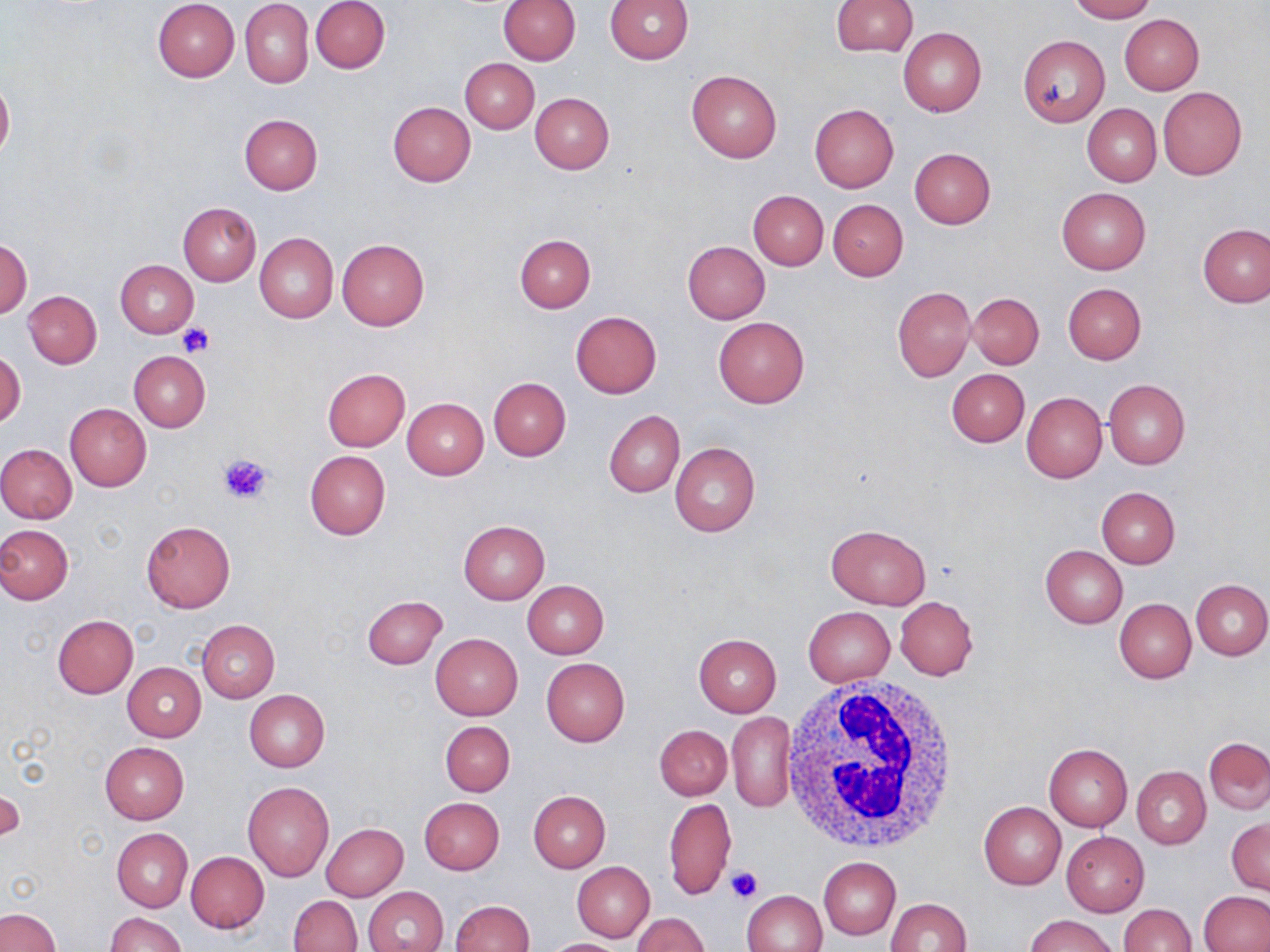

Approximate bounding boxes as (x1, y1, x2, y2) in pixels. Uninfected red blood cell locations: (152, 0, 240, 81), (312, 0, 390, 73), (498, 0, 581, 65), (606, 0, 695, 64), (831, 0, 918, 56), (1070, 0, 1154, 22), (241, 1, 313, 88), (1119, 15, 1204, 95), (898, 26, 986, 117), (1018, 36, 1109, 126), (460, 58, 539, 133), (686, 69, 782, 163), (0, 75, 13, 164), (1158, 87, 1247, 179), (531, 92, 614, 174), (388, 101, 475, 186), (809, 104, 898, 193), (1082, 104, 1161, 187), (239, 114, 323, 194), (909, 148, 996, 229), (1056, 187, 1151, 273), (748, 190, 828, 269), (828, 199, 908, 281), (179, 202, 260, 285), (1199, 224, 1269, 306), (255, 232, 337, 323), (514, 235, 595, 313), (0, 237, 32, 319), (337, 239, 430, 329), (682, 241, 770, 323), (115, 260, 198, 337), (1063, 282, 1147, 364), (892, 287, 975, 382), (24, 291, 101, 368), (969, 293, 1044, 369), (571, 311, 662, 398), (714, 316, 809, 407), (1, 350, 24, 429), (128, 351, 211, 432), (322, 369, 410, 451), (947, 369, 1028, 447), (488, 377, 571, 460), (1104, 378, 1190, 469), (1023, 392, 1107, 483), (402, 398, 488, 480), (65, 403, 151, 491), (604, 409, 685, 497), (670, 441, 761, 536), (0, 443, 77, 523), (305, 450, 391, 540), (1097, 486, 1179, 568), (458, 520, 550, 604), (141, 521, 235, 612), (826, 524, 931, 609), (0, 525, 73, 604), (1040, 544, 1127, 628), (1191, 579, 1270, 660), (523, 580, 608, 658), (362, 596, 447, 668), (895, 596, 979, 679), (1114, 598, 1196, 683), (803, 607, 895, 686), (52, 615, 138, 698), (197, 620, 280, 703), (431, 633, 522, 720), (693, 633, 781, 716), (542, 657, 630, 746), (122, 662, 205, 742), (245, 690, 329, 772), (727, 712, 796, 811), (440, 721, 515, 795), (655, 725, 732, 799), (1204, 736, 1270, 815), (100, 742, 189, 824), (1044, 743, 1132, 831), (1132, 765, 1210, 848), (243, 781, 334, 881), (2, 786, 23, 843), (528, 790, 610, 872), (419, 797, 505, 874), (664, 797, 736, 902), (979, 801, 1065, 889), (1227, 818, 1269, 894), (321, 823, 408, 900), (112, 829, 192, 911), (1062, 832, 1150, 916), (186, 851, 268, 933), (819, 857, 900, 939), (572, 861, 655, 942), (362, 886, 449, 952), (742, 890, 828, 952), (1200, 891, 1269, 951), (289, 895, 361, 951), (885, 898, 972, 951), (449, 900, 534, 952), (1118, 903, 1195, 952), (0, 908, 61, 952), (106, 912, 186, 952), (632, 913, 708, 951), (1024, 914, 1121, 952), (542, 939, 629, 951). Platelet locations: (177, 324, 214, 356), (218, 452, 274, 505), (725, 866, 761, 903). White blood cell locations: (780, 674, 959, 855). Slide-level diagnosis: no evidence of blood parasites. One field of a larger specimen. Optical microscopy. Thin blood smear. Image is 1270×952 pixels. May-Grünwald-Giemsa stain. Captured at 1000x magnification.